Give the extent of all Plasmodium falciparum-infected red blood cells.
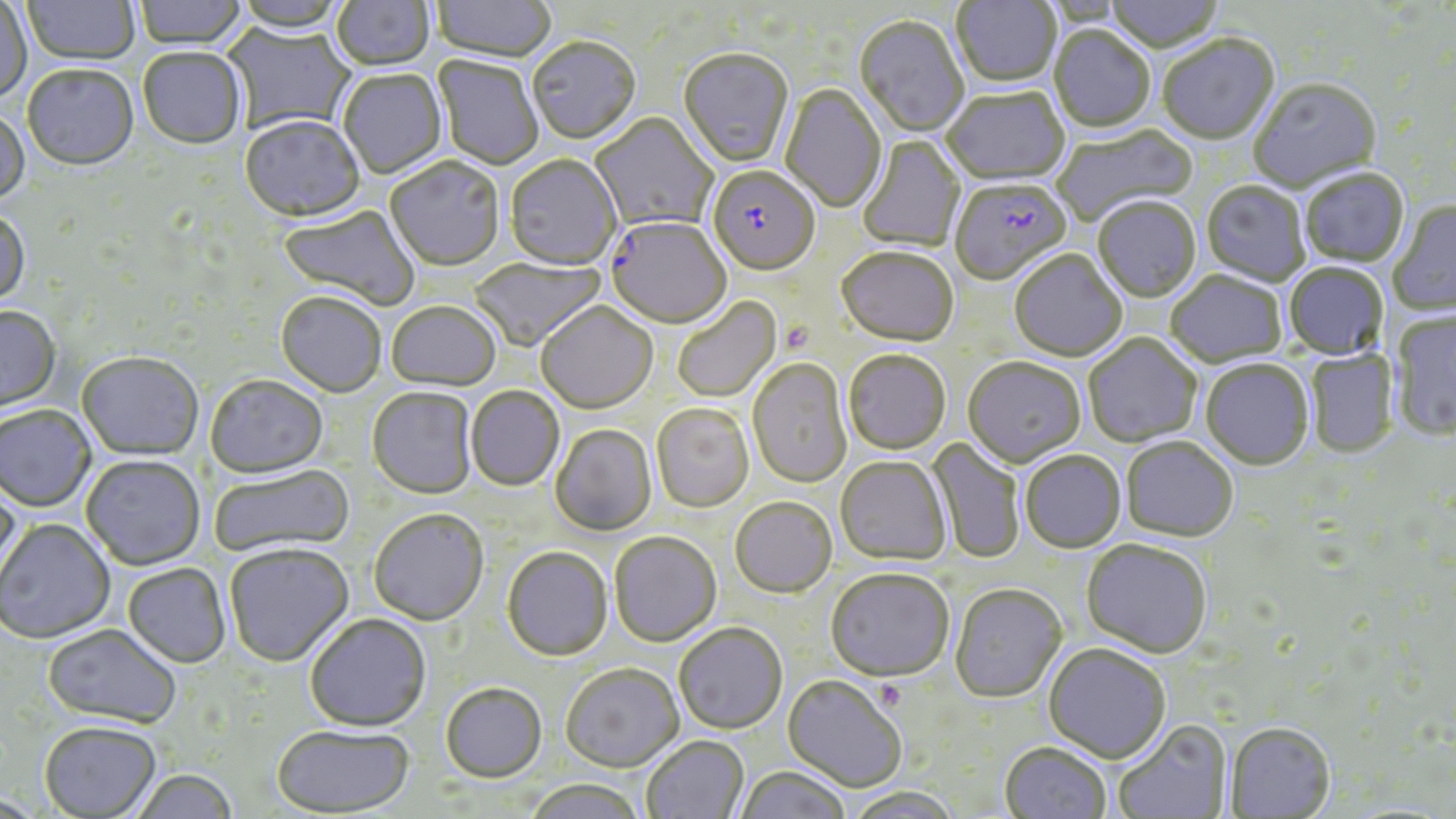
Approximate bounding boxes as (x1,y1)-(x2,y2) corner pairs in pixels.
Plasmodium falciparum-infected red blood cells: (707,168)-(820,277), (950,180)-(1071,287), (605,219)-(732,330).

slide-level diagnosis = Plasmodium falciparum
platelet locations = approximate bounding boxes as (x1,y1)-(x2,y2) corner pairs in pixels: (780,320)-(814,356)
stain = May-Grünwald-Giemsa
modality = optical microscopy
image size = 1456×819 pixels
magnification = 1000x
uninfected red blood cell locations = approximate bounding boxes as (x1,y1)-(x2,y2) corner pairs in pixels: (22,0)-(140,67), (134,0)-(246,51), (331,0)-(435,73), (952,0)-(1061,90), (1104,0)-(1225,55), (0,1)-(32,106), (432,1)-(556,64), (854,16)-(968,139), (222,23)-(355,135), (1049,27)-(1155,134), (1157,37)-(1279,146), (527,40)-(641,146), (137,49)-(247,151), (678,50)-(794,169), (433,56)-(543,171), (22,66)-(139,173), (338,71)-(446,179), (1249,80)-(1382,195), (780,84)-(887,214), (942,89)-(1070,187), (0,109)-(30,207), (591,114)-(717,232), (240,118)-(364,224), (1052,125)-(1198,226), (857,136)-(966,253), (504,156)-(621,272), (385,159)-(504,272), (1300,169)-(1410,269), (1201,182)-(1310,288), (1093,199)-(1201,304), (1389,201)-(1456,317), (278,204)-(421,311), (0,213)-(30,309), (836,250)-(958,348), (1009,251)-(1128,363), (469,258)-(605,352), (1284,263)-(1389,361), (1165,271)-(1288,368), (275,293)-(386,398), (672,298)-(781,402), (386,303)-(501,393), (536,303)-(658,415), (0,307)-(61,414), (1389,309)-(1456,442), (1083,334)-(1202,448), (1303,350)-(1399,458), (843,351)-(951,456), (76,354)-(204,461), (963,359)-(1086,468), (748,360)-(853,489), (1201,360)-(1314,470), (205,377)-(328,480), (466,387)-(565,491), (367,388)-(477,501), (651,405)-(754,513), (0,406)-(96,513), (551,425)-(657,536), (1120,437)-(1239,542), (927,438)-(1025,564), (1020,451)-(1126,553), (81,456)-(205,571), (835,458)-(952,566), (208,465)-(355,558), (0,477)-(22,588), (730,498)-(836,598), (369,510)-(489,627), (0,519)-(116,645), (609,532)-(722,648), (1081,540)-(1212,660), (224,544)-(354,668), (501,548)-(613,662), (123,564)-(231,669), (825,569)-(954,684), (950,585)-(1067,704), (305,615)-(432,733), (673,624)-(788,734), (42,625)-(181,729), (1043,644)-(1170,764), (560,665)-(685,774), (782,675)-(907,793), (441,685)-(546,784), (1113,720)-(1233,819), (39,723)-(162,818), (1225,723)-(1336,818), (271,727)-(415,817), (642,736)-(749,819), (999,742)-(1111,819), (734,766)-(852,819), (131,771)-(238,819), (524,779)-(645,819), (843,787)-(963,819)
field of view = single
preparation = thin blood smear